State the preparation type.
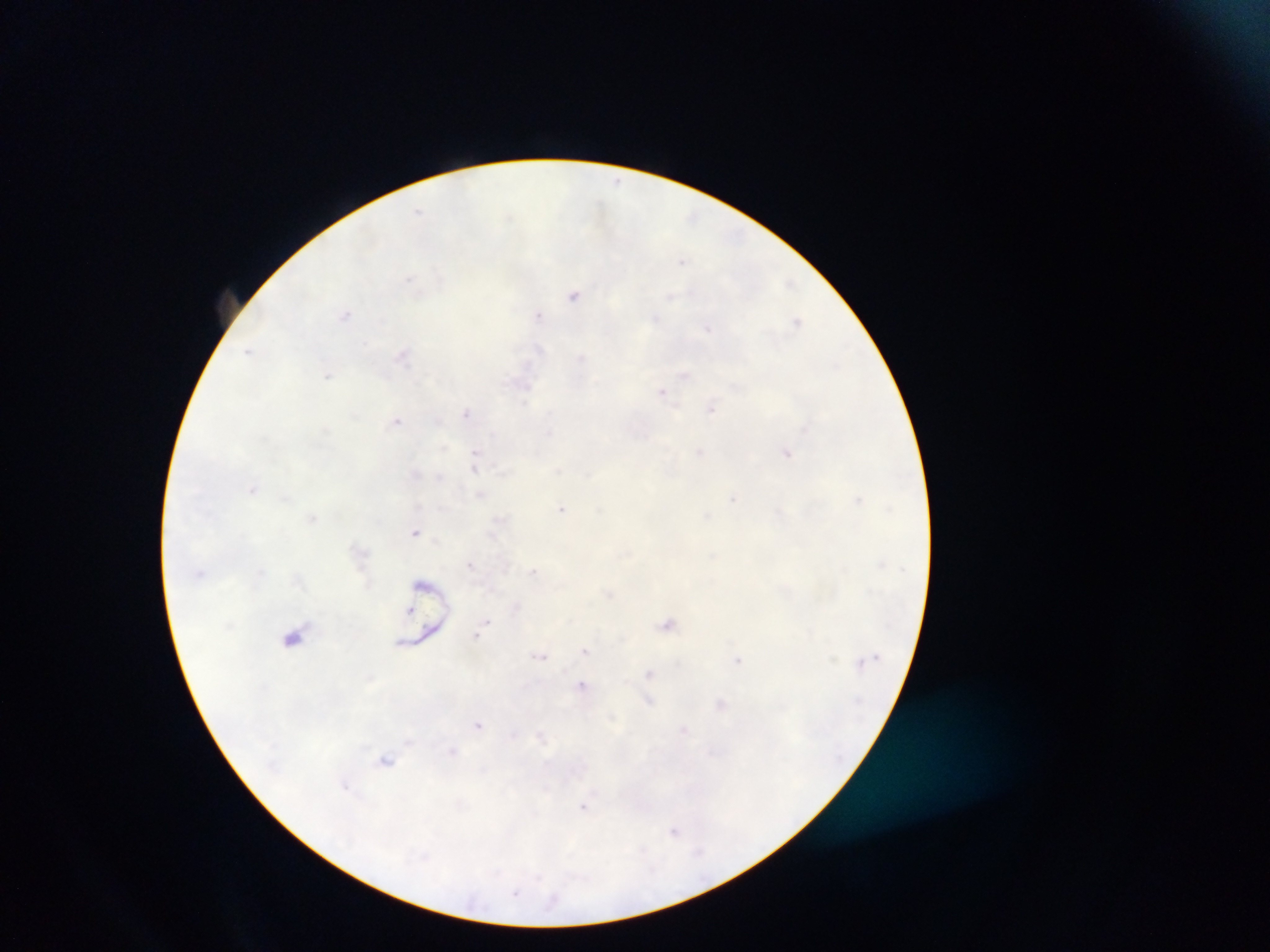

This is a thick smear.

malaria parasite locations = approximate centers as [x, y] in pixels: [617, 181], [419, 211], [693, 216], [682, 261], [409, 278], [575, 296], [670, 296], [345, 314], [538, 315], [655, 318], [796, 320], [708, 328], [365, 344], [249, 350], [404, 354], [581, 357], [685, 375], [329, 376], [662, 391], [712, 407], [467, 412], [396, 420], [548, 432], [787, 452], [699, 453], [476, 455], [475, 465], [416, 473], [253, 489], [480, 496], [285, 497], [733, 498], [858, 499], [562, 508], [707, 516], [312, 519], [415, 533], [492, 534], [470, 564], [533, 570], [261, 571], [609, 594], [515, 606], [486, 622], [668, 623], [476, 636], [293, 637], [586, 650], [539, 655], [738, 661], [650, 673], [582, 685], [648, 701], [720, 704], [478, 725], [684, 729], [513, 733], [540, 734], [453, 751], [387, 760], [347, 786], [584, 805], [674, 831], [699, 851], [516, 893]
capture = mobile-phone photograph through a microscope
country = Ghana
field of view = single
image size = 1270×952 pixels